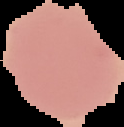
image type = segmented cell region on a black background
image size = 124×127 pixels
preparation = thin blood smear
result = no Plasmodium parasites seen